Name the parasite shown.
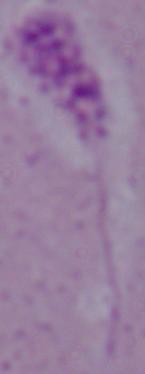

Leishmania.

Micrograph. Captured at 1000x magnification.